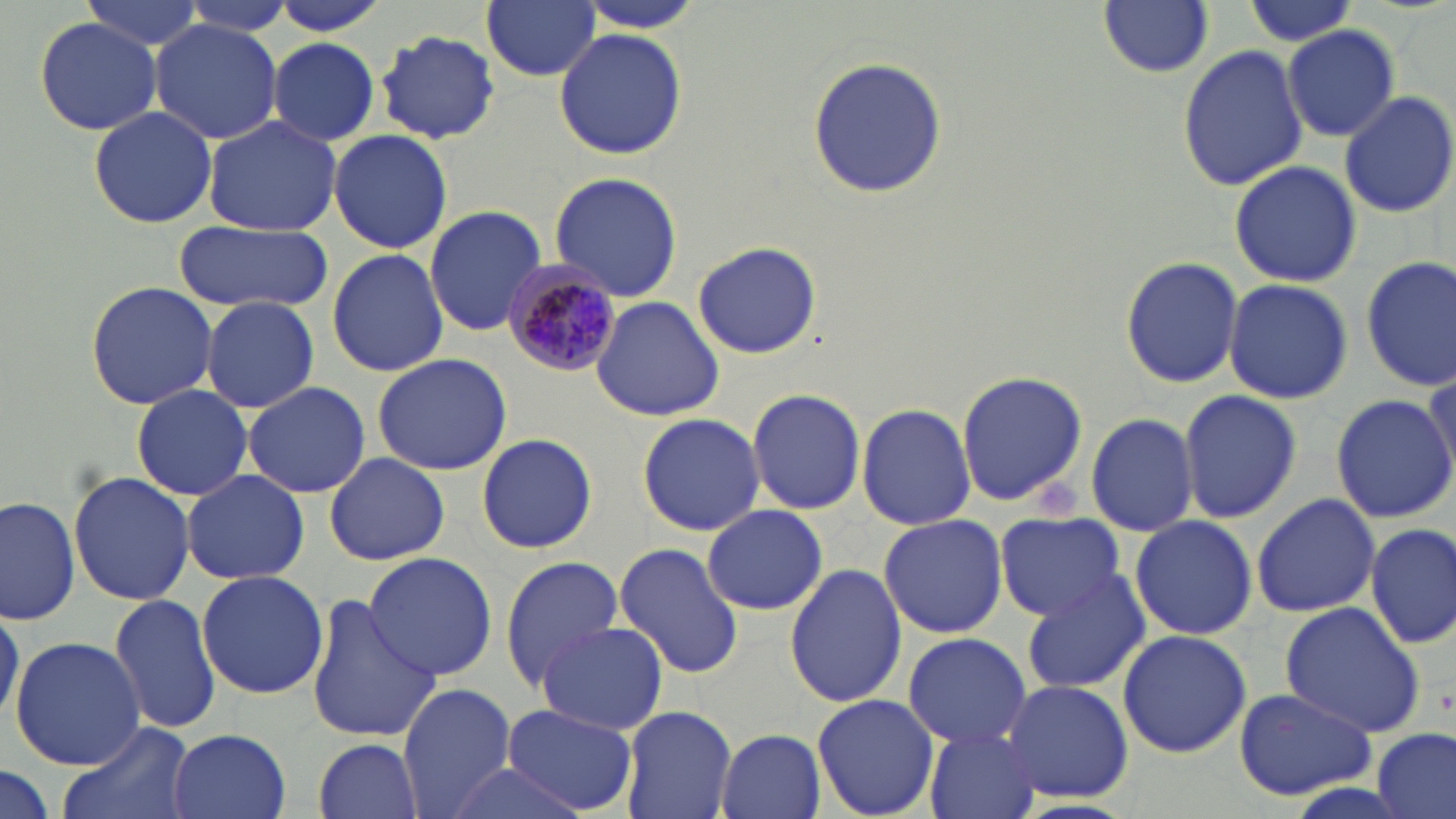
Summary:
  - Coordinate format: approximate bounding boxes as (x1, y1, x2, y2) in pixels
  - Plasmodium malariae-infected red blood cell locations: (500, 257, 623, 377)
  - Uninfected red blood cell locations: (264, 0, 392, 36), (482, 0, 601, 82), (1239, 0, 1360, 48), (80, 1, 207, 53), (1100, 1, 1213, 77), (171, 2, 295, 38), (34, 16, 162, 135), (147, 21, 284, 142), (1283, 25, 1398, 142), (555, 26, 688, 160), (375, 29, 503, 143), (268, 37, 380, 146), (1177, 46, 1310, 190), (807, 55, 947, 199), (1339, 90, 1456, 217), (87, 105, 219, 230), (203, 115, 341, 237), (329, 131, 453, 253), (1228, 160, 1360, 287), (549, 170, 684, 303), (424, 204, 549, 336), (173, 221, 333, 313), (691, 241, 821, 359), (327, 247, 449, 378), (1119, 255, 1244, 390), (1360, 257, 1456, 392), (84, 280, 221, 410), (1223, 280, 1352, 403), (590, 295, 725, 422), (200, 297, 320, 414), (371, 353, 514, 475), (954, 369, 1090, 507), (242, 380, 370, 499), (132, 386, 253, 500), (746, 388, 867, 514), (1177, 388, 1302, 523), (1330, 393, 1456, 523), (856, 405, 977, 533), (636, 412, 766, 536), (1085, 412, 1199, 537), (476, 433, 597, 555), (324, 451, 449, 565), (180, 469, 311, 585), (69, 470, 194, 608), (1251, 494, 1381, 618), (0, 497, 79, 627), (701, 503, 831, 616), (994, 511, 1128, 623), (878, 512, 1009, 640), (1129, 515, 1257, 641), (1364, 521, 1455, 649), (615, 541, 744, 680), (361, 552, 498, 682), (498, 556, 625, 690), (785, 565, 907, 708), (196, 571, 330, 699), (1020, 573, 1154, 692), (110, 594, 223, 733), (302, 594, 441, 745), (1280, 601, 1427, 739), (0, 602, 21, 734), (537, 620, 667, 735), (528, 627, 690, 819), (1116, 628, 1251, 759), (901, 631, 1031, 749), (11, 637, 146, 768), (1000, 678, 1134, 804), (397, 684, 519, 818), (1231, 688, 1375, 802), (811, 692, 940, 819), (505, 705, 638, 816), (620, 705, 737, 819), (58, 719, 193, 819), (922, 727, 1042, 819), (1374, 728, 1454, 819), (167, 729, 291, 819), (715, 729, 826, 819), (314, 737, 422, 819), (440, 760, 593, 817), (0, 763, 53, 817)
  - Platelet locations: (1037, 478, 1085, 525)
  - Slide-level diagnosis: Plasmodium malariae
  - Magnification: 1000x
  - Preparation: thin blood smear
  - Image size: 1456×819 pixels
  - Stain: May-Grünwald-Giemsa
  - Modality: light microscopy
  - Field of view: single